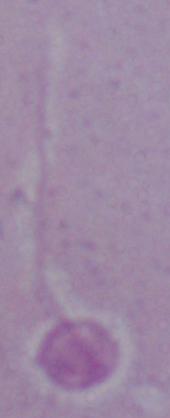

Summary:
  - Magnification: 1000x
  - Modality: photomicrograph
  - Identification: Leishmania